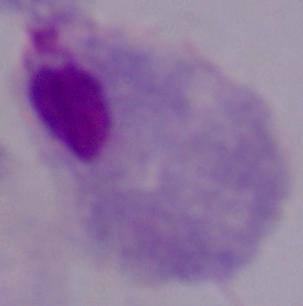
Captured at 1000x magnification. A trichomonad is seen. Photomicrograph.